State which parasite is depicted.
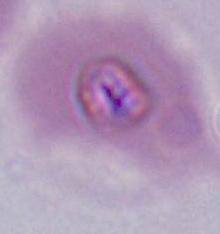
This is Plasmodium.

magnification = 400x or 1000x
modality = photomicrograph